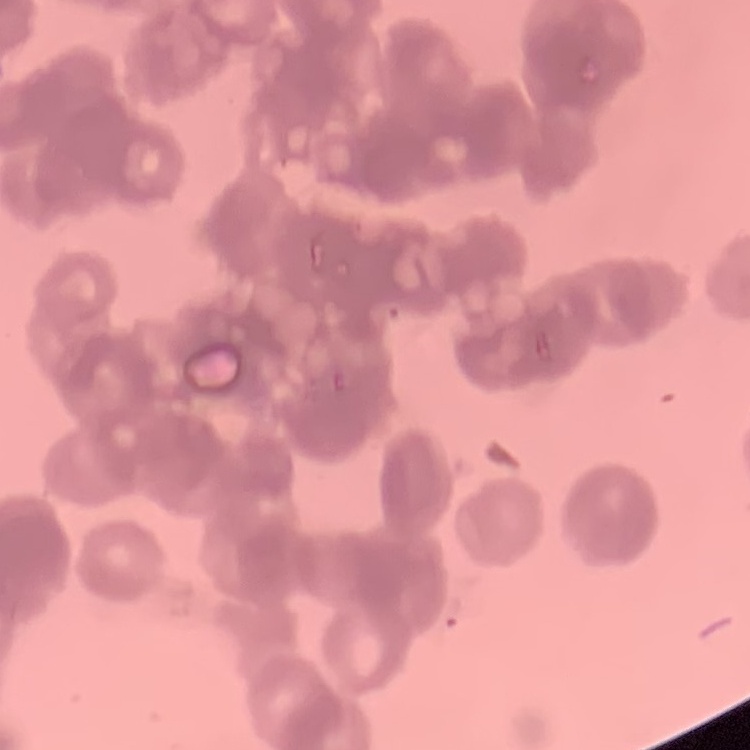
Summary:
  - Erythrocyte morphology: rouleaux formation
  - Image type: square crop of a larger photomicrograph
  - Stain: Field's or Giemsa
  - Preparation: thin peripheral smear